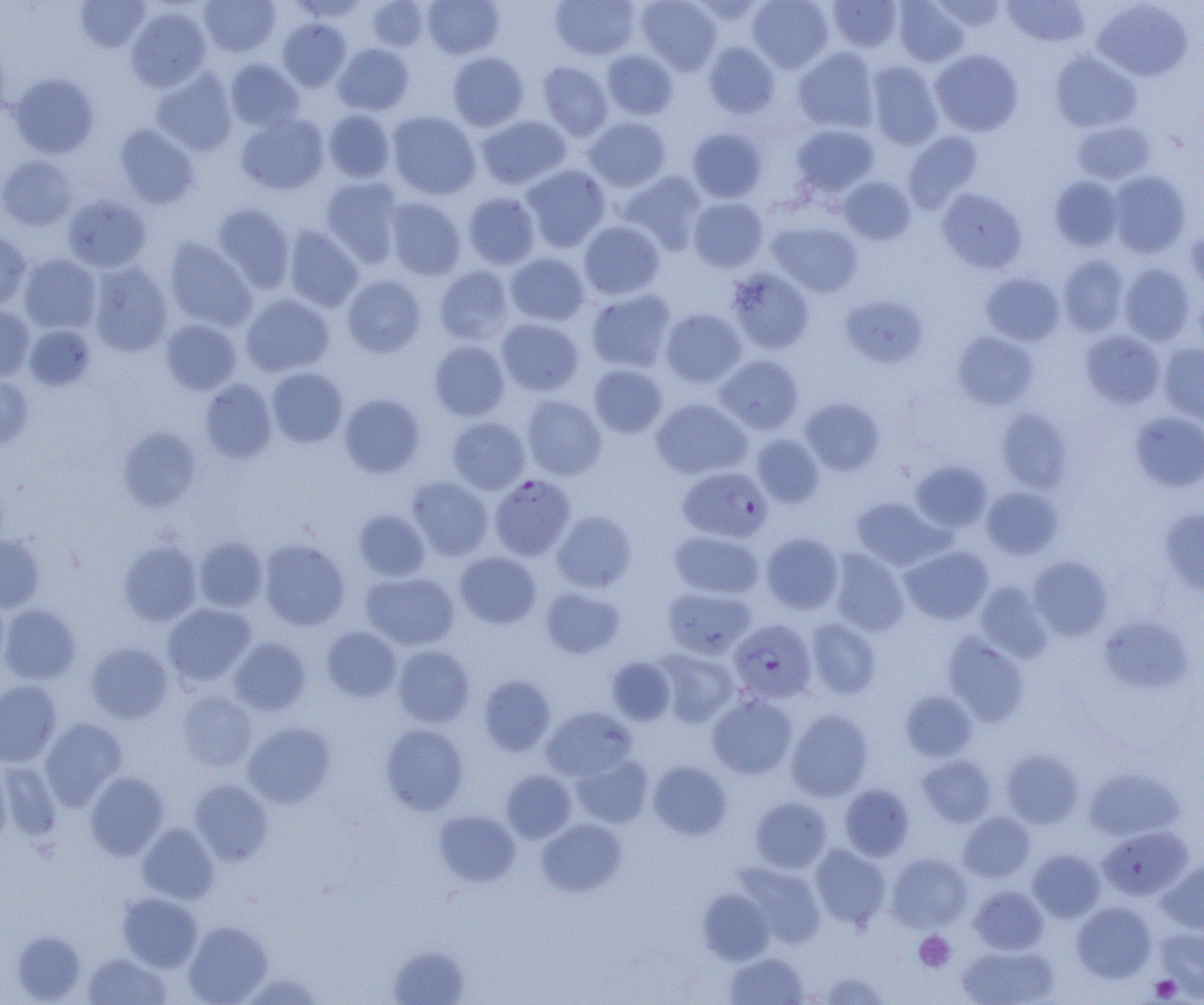
Summary:
  - Coordinate format: approximate bounding boxes as (x1, y1, x2, y2) in pixels
  - Uninfected red blood cell locations: (74, 0, 151, 52), (199, 0, 281, 57), (289, 0, 370, 21), (422, 0, 504, 59), (550, 0, 640, 60), (636, 0, 722, 75), (747, 0, 834, 73), (893, 0, 969, 66), (1003, 0, 1091, 47), (366, 1, 429, 51), (827, 1, 903, 52), (931, 1, 1009, 32), (1092, 1, 1193, 81), (126, 6, 211, 91), (278, 18, 351, 91), (703, 41, 780, 118), (333, 43, 414, 115), (793, 47, 879, 132), (602, 49, 678, 120), (930, 50, 1023, 137), (1050, 50, 1141, 133), (447, 51, 529, 131), (225, 58, 303, 131), (537, 61, 614, 140), (866, 61, 944, 150), (151, 68, 238, 156), (9, 73, 99, 158), (323, 109, 396, 183), (386, 111, 481, 200), (235, 112, 329, 195), (476, 115, 572, 190), (584, 116, 672, 191), (1072, 120, 1155, 184), (791, 123, 879, 197), (114, 124, 200, 209), (687, 127, 767, 203), (903, 131, 984, 213), (0, 155, 77, 231), (520, 164, 611, 252), (619, 170, 707, 254), (1108, 170, 1190, 257), (838, 175, 916, 245), (1049, 175, 1124, 250), (321, 177, 404, 267), (937, 188, 1027, 273), (463, 191, 541, 269), (62, 194, 152, 272), (687, 196, 768, 272), (384, 197, 466, 280), (212, 203, 294, 292), (578, 220, 665, 300), (767, 221, 863, 298), (282, 225, 363, 311), (1185, 230, 1204, 295), (0, 234, 32, 311), (163, 237, 257, 331), (504, 252, 591, 326), (18, 254, 101, 334), (1059, 255, 1130, 336), (88, 262, 173, 357), (1119, 263, 1195, 345), (433, 265, 515, 345), (725, 268, 815, 355), (981, 273, 1065, 346), (341, 275, 426, 357), (587, 288, 676, 372), (241, 294, 334, 376), (838, 295, 928, 368), (0, 306, 35, 380), (660, 307, 747, 388), (496, 318, 584, 396), (160, 319, 242, 395), (23, 324, 96, 390), (1079, 330, 1165, 409), (951, 331, 1039, 410), (429, 340, 510, 421), (1159, 343, 1204, 426), (714, 355, 804, 435), (589, 364, 668, 438), (266, 367, 348, 447), (0, 374, 33, 450), (199, 379, 277, 463), (338, 393, 425, 479), (522, 395, 606, 480), (651, 398, 752, 480), (800, 398, 884, 475), (995, 408, 1073, 493), (1130, 411, 1204, 492), (447, 416, 530, 494), (118, 427, 201, 512), (752, 434, 824, 507), (910, 461, 992, 532), (407, 476, 493, 560), (981, 486, 1063, 560), (851, 496, 944, 570), (352, 509, 431, 581), (1159, 509, 1204, 595), (552, 510, 637, 593), (669, 530, 764, 599), (760, 531, 844, 614), (0, 535, 45, 612), (194, 536, 268, 611), (258, 539, 350, 630), (118, 540, 202, 626), (901, 546, 993, 624), (828, 548, 909, 636), (455, 551, 541, 629), (1028, 556, 1113, 640), (360, 572, 459, 650), (977, 582, 1053, 661), (663, 586, 758, 659), (540, 587, 624, 658), (162, 603, 255, 686), (0, 604, 81, 684), (1100, 616, 1194, 693), (804, 617, 881, 700), (321, 626, 402, 702), (943, 634, 1028, 725), (228, 637, 310, 716), (86, 642, 172, 723), (392, 645, 475, 728), (653, 649, 738, 727), (607, 656, 676, 724), (478, 675, 555, 756), (0, 680, 61, 766), (177, 690, 257, 770), (900, 690, 978, 762), (707, 693, 797, 779), (541, 706, 637, 781), (786, 708, 873, 801), (39, 718, 126, 808), (243, 722, 335, 808), (380, 723, 469, 815), (1002, 750, 1084, 828), (572, 753, 652, 828), (918, 755, 996, 827), (0, 760, 62, 841), (648, 761, 732, 840), (0, 762, 12, 848), (1083, 767, 1185, 840), (501, 770, 576, 842), (85, 772, 169, 859), (189, 779, 273, 865), (839, 783, 914, 860), (750, 797, 832, 872), (434, 810, 520, 887), (958, 812, 1035, 883), (536, 818, 627, 897), (137, 824, 219, 904), (1097, 826, 1191, 901), (810, 844, 891, 929), (1027, 848, 1105, 922), (887, 853, 972, 931), (1159, 857, 1204, 934), (736, 863, 825, 948), (969, 885, 1048, 954), (698, 889, 774, 965), (117, 893, 202, 971), (1072, 902, 1157, 982), (183, 920, 272, 1004), (1155, 927, 1204, 1001), (12, 929, 86, 1003), (388, 944, 470, 1004), (957, 944, 1059, 1005), (83, 952, 171, 1004), (724, 952, 809, 1005), (814, 972, 892, 1004)
  - Platelet locations: (914, 931, 955, 972), (1150, 975, 1181, 1002)
  - Plasmodium falciparum-infected red blood cell locations: (678, 466, 773, 543), (489, 474, 576, 560), (728, 619, 816, 704)
  - Slide-level diagnosis: Plasmodium falciparum
  - Field of view: single
  - Magnification: 1000x
  - Modality: light microscopy
  - Image size: 1204×1005 pixels
  - Preparation: thin blood film